Identify the parasite.
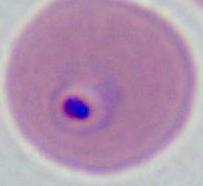

Plasmodium.

Summary:
  - Magnification: 400x or 1000x
  - Modality: photomicrograph